Outline platelets.
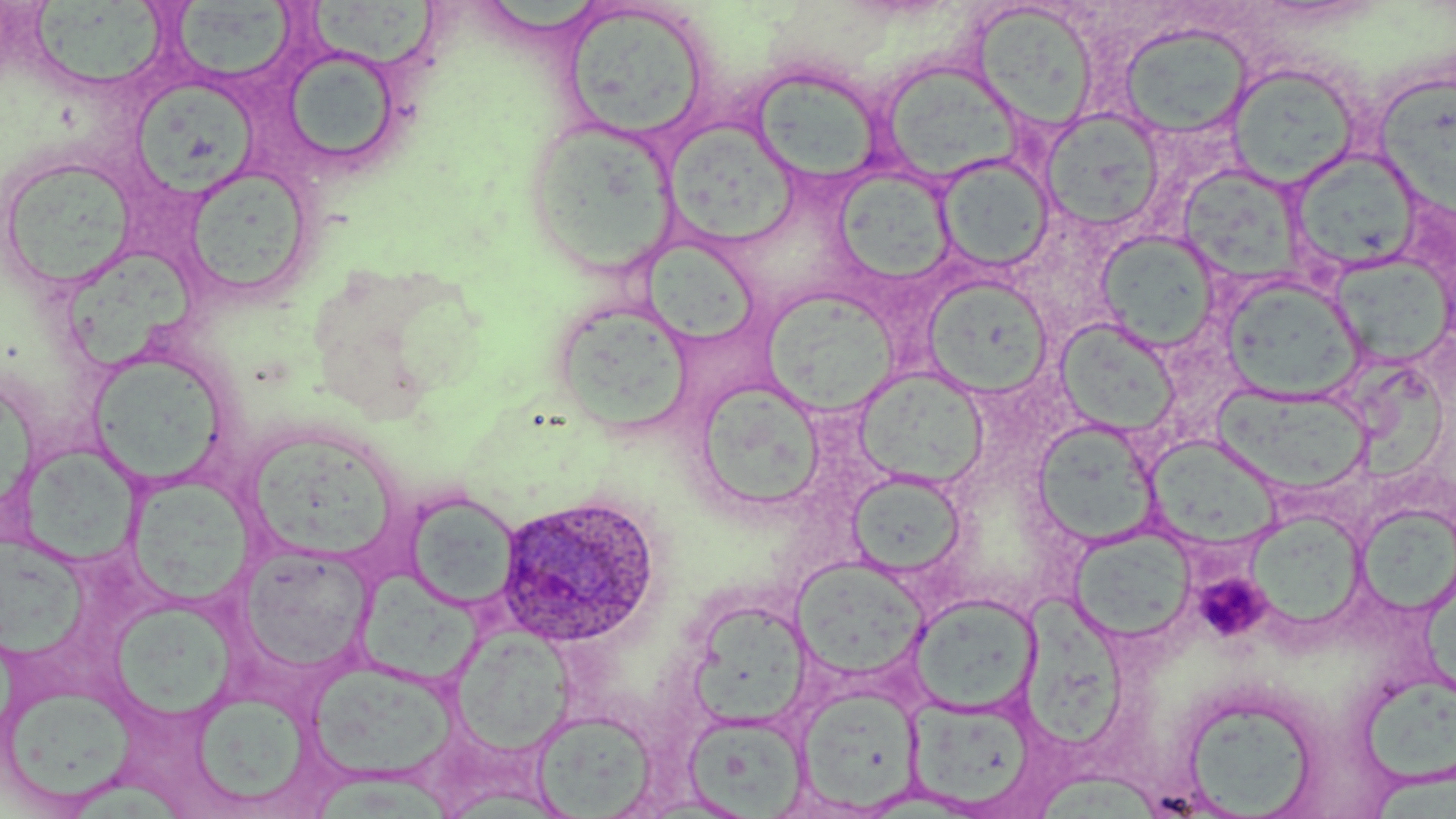

Approximate bounding boxes as named x1/y1/x2/y2 corners in pixels.
Platelets: (x1=1192, y1=571, x2=1274, y2=643), (x1=1193, y1=572, x2=1273, y2=642).

Summary:
  - Uninfected red blood cell locations: (x1=35, y1=0, x2=173, y2=88), (x1=310, y1=0, x2=449, y2=69), (x1=562, y1=2, x2=713, y2=142), (x1=970, y1=3, x2=1100, y2=133), (x1=168, y1=4, x2=300, y2=84), (x1=1117, y1=23, x2=1255, y2=139), (x1=279, y1=49, x2=401, y2=175), (x1=880, y1=59, x2=1026, y2=186), (x1=1225, y1=63, x2=1362, y2=190), (x1=750, y1=66, x2=886, y2=188), (x1=1376, y1=74, x2=1455, y2=216), (x1=126, y1=80, x2=263, y2=206), (x1=1040, y1=109, x2=1165, y2=233), (x1=522, y1=117, x2=678, y2=275), (x1=665, y1=121, x2=800, y2=248), (x1=1288, y1=149, x2=1423, y2=276), (x1=1, y1=152, x2=138, y2=295), (x1=936, y1=154, x2=1055, y2=274), (x1=182, y1=163, x2=316, y2=304), (x1=1177, y1=165, x2=1304, y2=284), (x1=833, y1=167, x2=958, y2=289), (x1=1096, y1=231, x2=1220, y2=351), (x1=642, y1=236, x2=759, y2=347), (x1=68, y1=241, x2=193, y2=375), (x1=1329, y1=255, x2=1452, y2=369), (x1=923, y1=276, x2=1052, y2=397), (x1=1220, y1=276, x2=1364, y2=403), (x1=763, y1=293, x2=908, y2=418), (x1=549, y1=298, x2=694, y2=434), (x1=1056, y1=318, x2=1182, y2=438), (x1=87, y1=349, x2=232, y2=490), (x1=1351, y1=362, x2=1445, y2=486), (x1=853, y1=367, x2=989, y2=489), (x1=695, y1=380, x2=828, y2=514), (x1=1214, y1=385, x2=1373, y2=496), (x1=1031, y1=419, x2=1159, y2=547), (x1=243, y1=438, x2=408, y2=570), (x1=17, y1=448, x2=149, y2=569), (x1=127, y1=470, x2=261, y2=607), (x1=848, y1=472, x2=966, y2=578), (x1=404, y1=491, x2=520, y2=611), (x1=1355, y1=504, x2=1456, y2=617), (x1=1244, y1=511, x2=1367, y2=632), (x1=1069, y1=528, x2=1195, y2=644), (x1=0, y1=537, x2=94, y2=667), (x1=238, y1=544, x2=375, y2=677), (x1=791, y1=558, x2=930, y2=683), (x1=363, y1=572, x2=491, y2=687), (x1=907, y1=593, x2=1041, y2=717), (x1=1024, y1=593, x2=1134, y2=750), (x1=692, y1=605, x2=802, y2=726), (x1=115, y1=606, x2=248, y2=730), (x1=453, y1=629, x2=576, y2=754), (x1=308, y1=661, x2=456, y2=785), (x1=1362, y1=680, x2=1456, y2=785), (x1=2, y1=681, x2=135, y2=809), (x1=797, y1=685, x2=923, y2=812), (x1=1175, y1=690, x2=1321, y2=817), (x1=187, y1=693, x2=322, y2=809), (x1=907, y1=696, x2=1040, y2=813), (x1=531, y1=709, x2=658, y2=818), (x1=683, y1=712, x2=810, y2=817), (x1=1367, y1=757, x2=1456, y2=819), (x1=1038, y1=772, x2=1161, y2=819)
  - Plasmodium ovale-infected red blood cell locations: (x1=496, y1=493, x2=663, y2=649)
  - Slide-level diagnosis: Plasmodium ovale
  - Magnification: 1000x
  - Modality: light microscopy
  - Field of view: one of a larger specimen
  - Stain: May-Grünwald-Giemsa
  - Preparation: thin blood smear
  - Image size: 1456×819 pixels